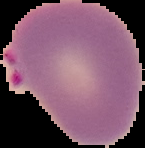

preparation = thin blood smear
image type = cell region segmented out of the field of view; surrounding area masked to black
malaria status = parasitized
image size = 145×148 pixels